Give the extent of all Plasmodium falciparum-infected red blood cells.
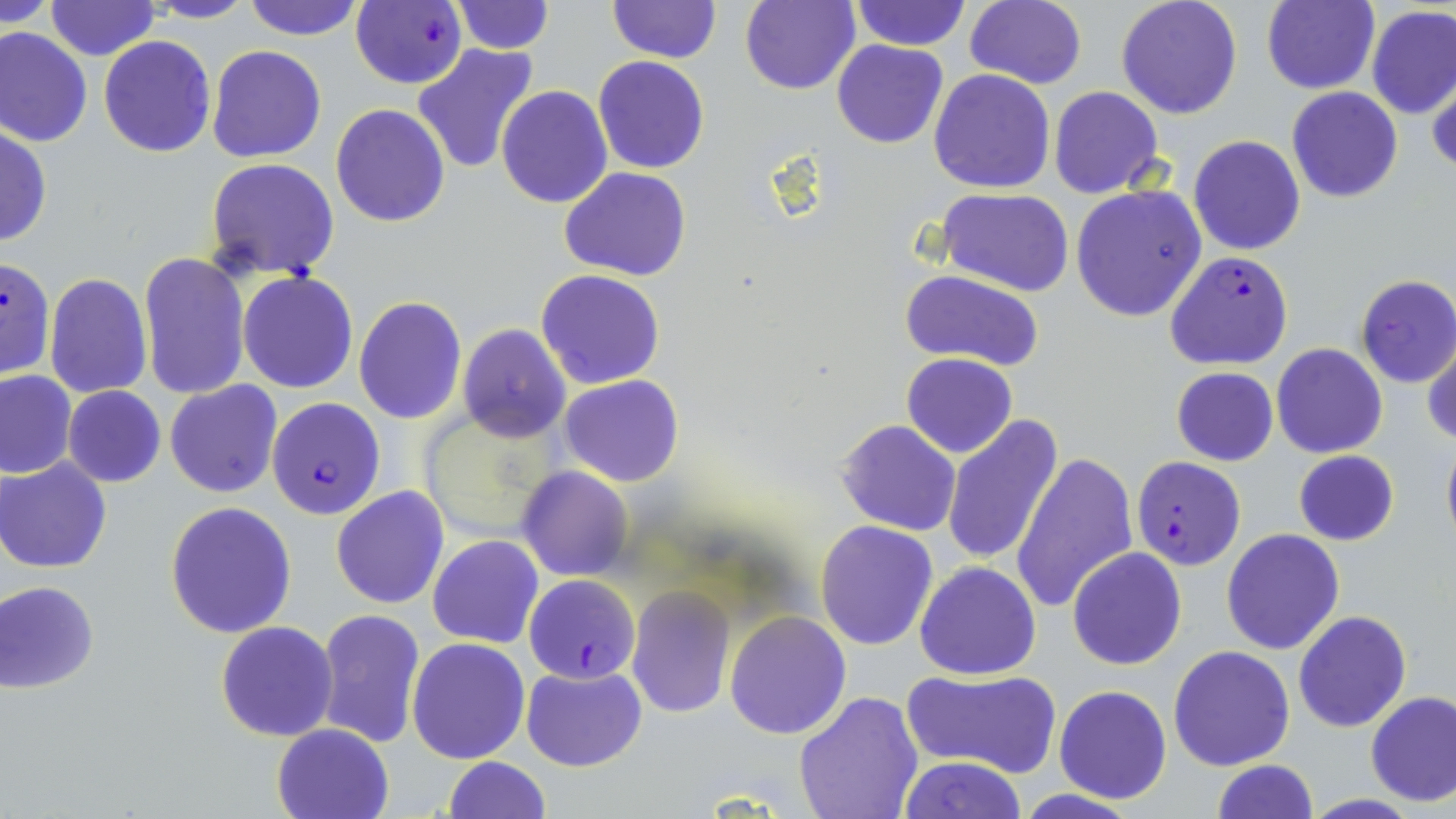

Approximate bounding boxes as named x1/y1/x2/y2 corners in pixels.
Plasmodium falciparum-infected red blood cells: (x1=350, y1=1, x2=467, y2=89), (x1=1165, y1=251, x2=1294, y2=370), (x1=0, y1=257, x2=55, y2=380), (x1=263, y1=399, x2=386, y2=522), (x1=1132, y1=455, x2=1246, y2=570), (x1=525, y1=575, x2=640, y2=685).

Uninfected red blood cell locations: (x1=3, y1=0, x2=56, y2=30), (x1=143, y1=0, x2=256, y2=22), (x1=243, y1=0, x2=364, y2=41), (x1=850, y1=0, x2=969, y2=49), (x1=964, y1=0, x2=1087, y2=88), (x1=1115, y1=0, x2=1243, y2=120), (x1=44, y1=1, x2=161, y2=62), (x1=450, y1=1, x2=553, y2=54), (x1=606, y1=1, x2=721, y2=65), (x1=739, y1=1, x2=860, y2=94), (x1=1261, y1=1, x2=1379, y2=95), (x1=1365, y1=6, x2=1456, y2=119), (x1=0, y1=26, x2=93, y2=147), (x1=98, y1=36, x2=215, y2=157), (x1=831, y1=39, x2=948, y2=149), (x1=413, y1=43, x2=541, y2=176), (x1=206, y1=45, x2=328, y2=163), (x1=593, y1=55, x2=708, y2=174), (x1=1427, y1=68, x2=1456, y2=178), (x1=928, y1=70, x2=1056, y2=193), (x1=1049, y1=85, x2=1164, y2=198), (x1=1286, y1=86, x2=1403, y2=203), (x1=497, y1=87, x2=613, y2=209), (x1=330, y1=104, x2=450, y2=228), (x1=0, y1=124, x2=51, y2=248), (x1=1188, y1=135, x2=1306, y2=256), (x1=206, y1=158, x2=340, y2=280), (x1=560, y1=167, x2=693, y2=280), (x1=1071, y1=185, x2=1207, y2=322), (x1=937, y1=188, x2=1075, y2=295), (x1=138, y1=251, x2=250, y2=399), (x1=536, y1=269, x2=667, y2=390), (x1=899, y1=270, x2=1045, y2=373), (x1=44, y1=271, x2=153, y2=400), (x1=238, y1=272, x2=358, y2=392), (x1=1354, y1=276, x2=1456, y2=389), (x1=353, y1=297, x2=467, y2=423), (x1=456, y1=323, x2=572, y2=443), (x1=1424, y1=339, x2=1456, y2=449), (x1=1272, y1=344, x2=1388, y2=459), (x1=901, y1=353, x2=1017, y2=457), (x1=1170, y1=367, x2=1279, y2=466), (x1=0, y1=371, x2=76, y2=478), (x1=560, y1=374, x2=685, y2=487), (x1=165, y1=381, x2=282, y2=497), (x1=62, y1=385, x2=166, y2=487), (x1=942, y1=415, x2=1063, y2=569), (x1=836, y1=420, x2=961, y2=536), (x1=1440, y1=435, x2=1456, y2=554), (x1=1293, y1=449, x2=1399, y2=546), (x1=1011, y1=450, x2=1138, y2=614), (x1=0, y1=458, x2=111, y2=573), (x1=515, y1=466, x2=633, y2=581), (x1=331, y1=486, x2=448, y2=609), (x1=165, y1=501, x2=296, y2=638), (x1=815, y1=519, x2=939, y2=651), (x1=1221, y1=528, x2=1345, y2=655), (x1=428, y1=534, x2=544, y2=648), (x1=1067, y1=548, x2=1188, y2=670), (x1=914, y1=562, x2=1041, y2=680), (x1=1, y1=580, x2=100, y2=693), (x1=626, y1=585, x2=736, y2=720), (x1=315, y1=608, x2=425, y2=748), (x1=1293, y1=609, x2=1411, y2=731), (x1=724, y1=610, x2=852, y2=739), (x1=214, y1=620, x2=339, y2=741), (x1=406, y1=637, x2=531, y2=764), (x1=1167, y1=645, x2=1296, y2=771), (x1=521, y1=664, x2=647, y2=772), (x1=902, y1=667, x2=1063, y2=779), (x1=1054, y1=685, x2=1173, y2=802), (x1=1365, y1=690, x2=1456, y2=806), (x1=793, y1=691, x2=925, y2=819), (x1=271, y1=722, x2=395, y2=819), (x1=442, y1=755, x2=549, y2=819), (x1=898, y1=755, x2=1027, y2=819), (x1=1211, y1=760, x2=1318, y2=818). Slide-level diagnosis: Plasmodium falciparum. Optical microscopy. Thin blood smear. May-Grünwald-Giemsa-stained preparation. Image is 1456×819 pixels. One field of a larger specimen. 1000x magnification.